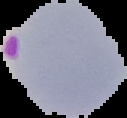

Summary:
  - Preparation: thin blood smear
  - Image type: segmented cell region on a black background
  - Malaria status: parasitized
  - Image size: 127×118 pixels